State the preparation type.
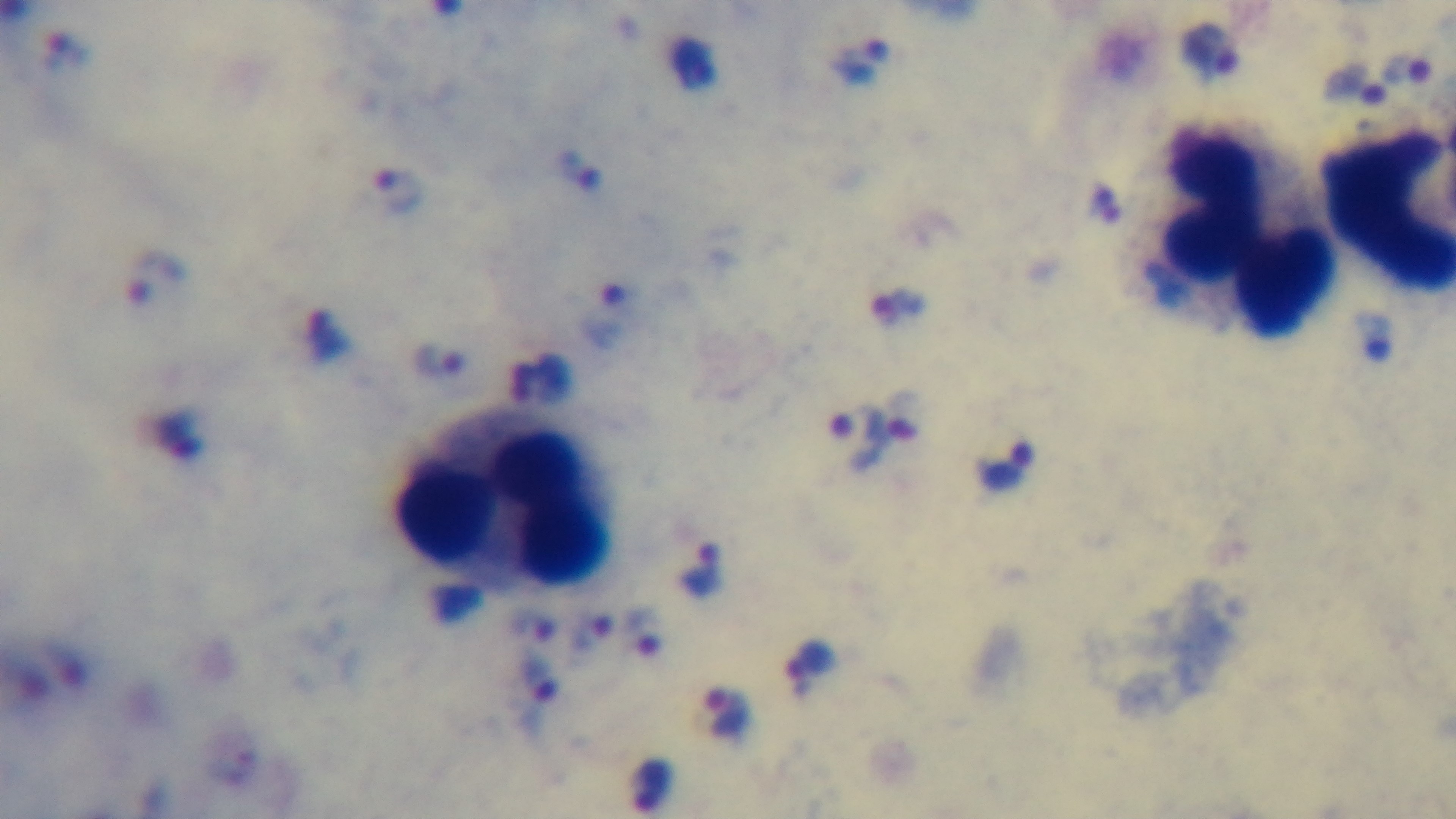
Thick.

100x oil-immersion objective. Mounted 4K digital camera. Single field of view. Malaria status: positive. Giemsa-stained. Photomicrograph.